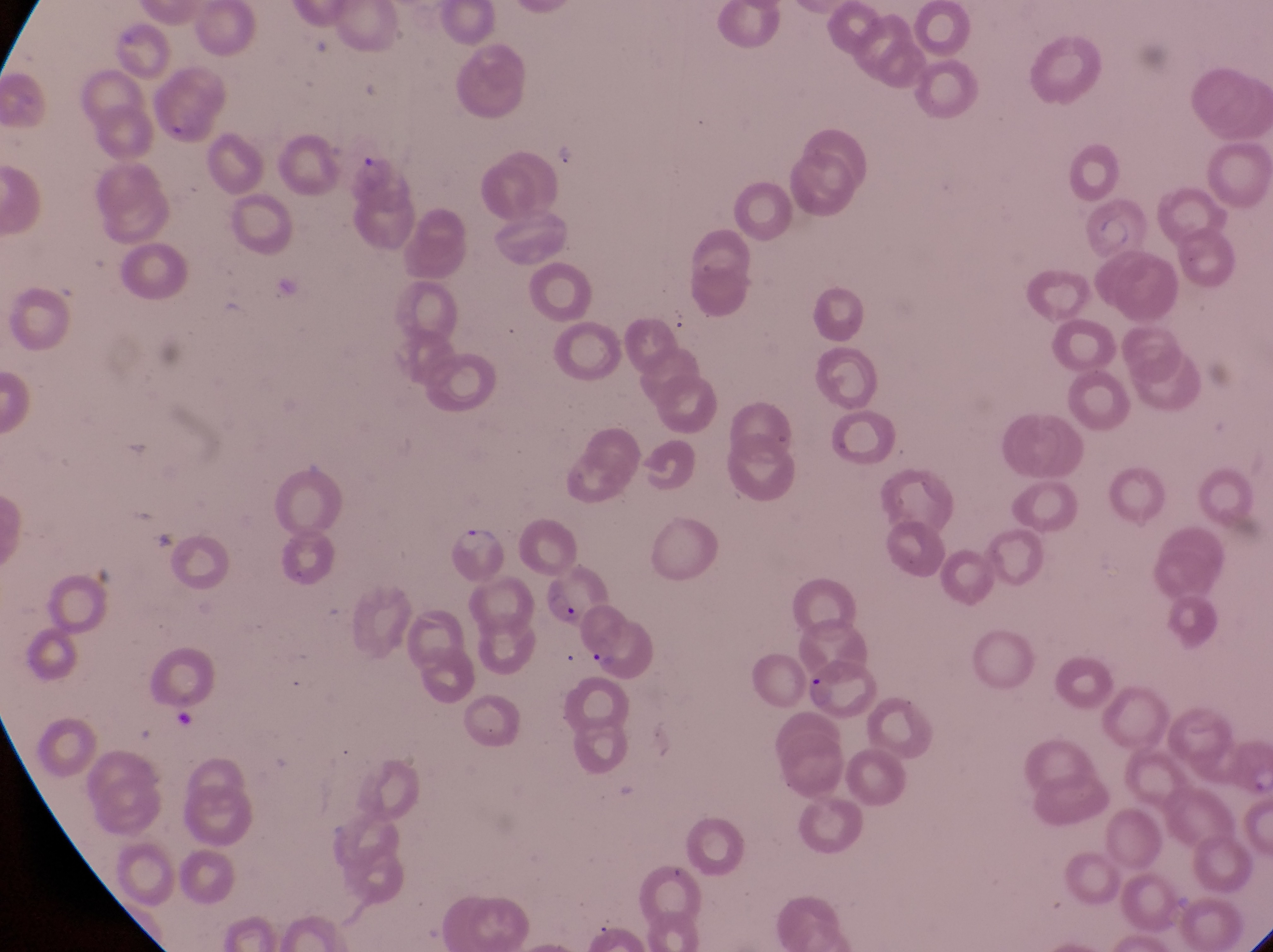

Approximate bounding boxes as left top right bottom in pixels. Trophozoite locations: 449 519 497 559. Parasitised red blood cell locations: 352 150 417 215; 1086 200 1166 263; 544 574 606 629; 572 607 650 684; 808 654 885 724. Thin blood smear. Photographed through the eyepiece of an Olympus CX-23 microscope with a smartphone camera. Magnification of 1000x. Collected in Uganda. Image is 1273×952 pixels. One field of view.